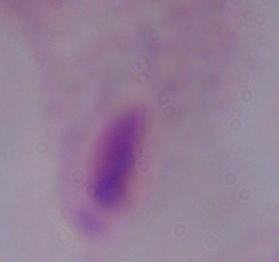
identification = trichomonad
modality = photomicrograph
magnification = 1000x